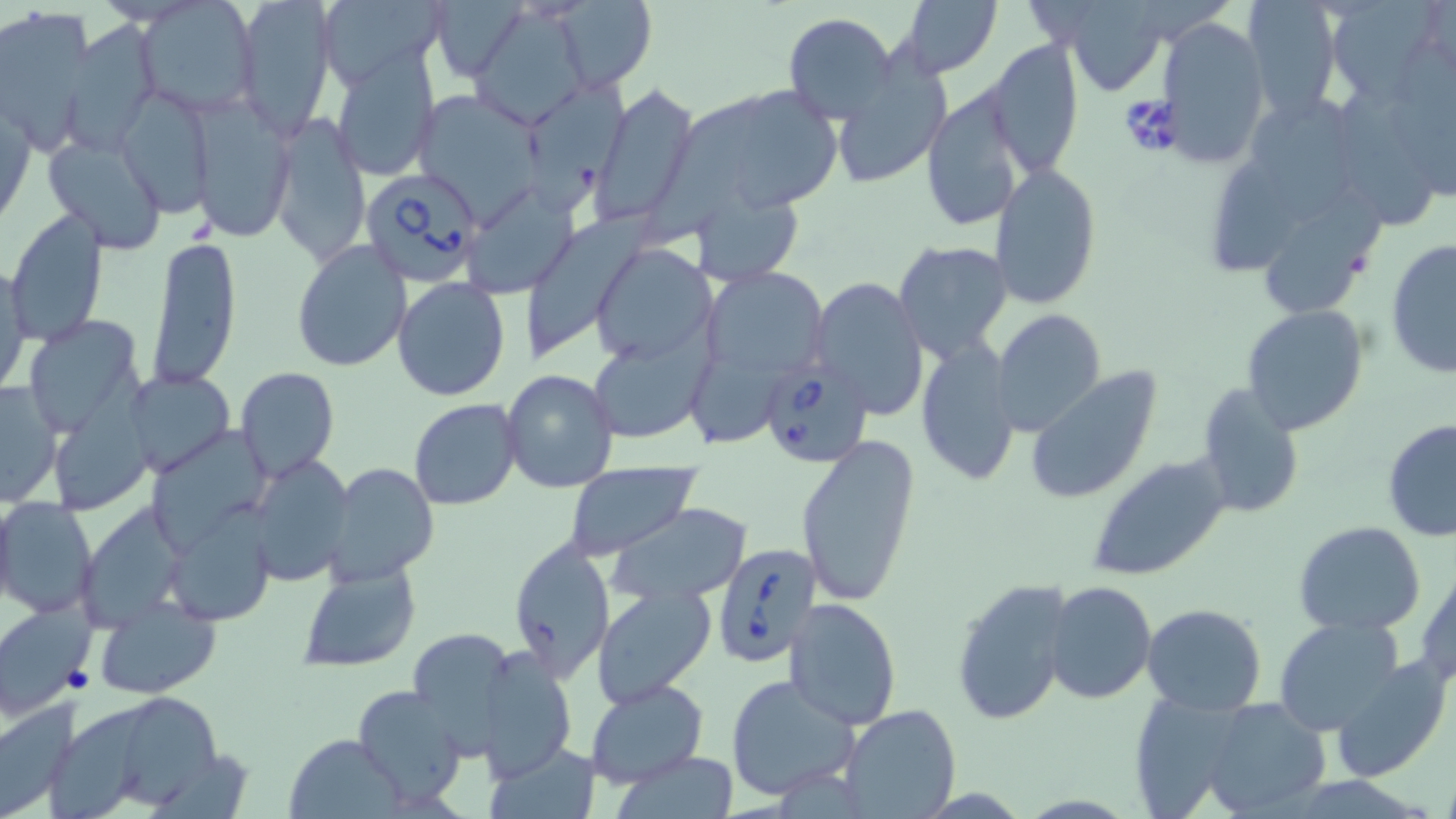
Summary:
  - Coordinate format: approximate bounding boxes as named x1/y1/x2/y2 corners in pixels
  - Uninfected red blood cell locations: (x1=135, y1=0, x2=263, y2=115), (x1=232, y1=0, x2=336, y2=140), (x1=318, y1=0, x2=442, y2=89), (x1=430, y1=0, x2=529, y2=83), (x1=547, y1=0, x2=658, y2=92), (x1=897, y1=0, x2=1002, y2=78), (x1=1239, y1=0, x2=1343, y2=119), (x1=1326, y1=0, x2=1450, y2=104), (x1=1050, y1=1, x2=1172, y2=94), (x1=470, y1=5, x2=590, y2=129), (x1=0, y1=8, x2=93, y2=154), (x1=784, y1=13, x2=898, y2=122), (x1=1155, y1=18, x2=1268, y2=165), (x1=62, y1=22, x2=159, y2=151), (x1=985, y1=39, x2=1083, y2=179), (x1=1391, y1=43, x2=1456, y2=200), (x1=333, y1=46, x2=441, y2=180), (x1=830, y1=56, x2=953, y2=190), (x1=520, y1=67, x2=628, y2=224), (x1=592, y1=82, x2=698, y2=223), (x1=114, y1=89, x2=214, y2=217), (x1=689, y1=89, x2=845, y2=212), (x1=921, y1=89, x2=1030, y2=231), (x1=425, y1=92, x2=541, y2=230), (x1=1337, y1=92, x2=1432, y2=229), (x1=0, y1=93, x2=35, y2=230), (x1=187, y1=97, x2=298, y2=243), (x1=1249, y1=98, x2=1353, y2=224), (x1=946, y1=101, x2=1090, y2=265), (x1=268, y1=112, x2=371, y2=268), (x1=42, y1=136, x2=167, y2=254), (x1=1211, y1=162, x2=1299, y2=272), (x1=989, y1=163, x2=1102, y2=309), (x1=459, y1=179, x2=579, y2=296), (x1=691, y1=185, x2=807, y2=287), (x1=1264, y1=188, x2=1387, y2=318), (x1=530, y1=211, x2=661, y2=363), (x1=6, y1=212, x2=111, y2=344), (x1=1386, y1=236, x2=1455, y2=380), (x1=146, y1=237, x2=241, y2=391), (x1=291, y1=240, x2=412, y2=372), (x1=893, y1=240, x2=1014, y2=363), (x1=590, y1=244, x2=717, y2=366), (x1=0, y1=257, x2=31, y2=402), (x1=703, y1=265, x2=828, y2=388), (x1=393, y1=276, x2=511, y2=400), (x1=809, y1=277, x2=930, y2=418), (x1=1240, y1=304, x2=1369, y2=434), (x1=991, y1=308, x2=1105, y2=436), (x1=23, y1=312, x2=147, y2=434), (x1=586, y1=331, x2=709, y2=447), (x1=916, y1=334, x2=1019, y2=485), (x1=692, y1=355, x2=782, y2=446), (x1=234, y1=366, x2=340, y2=480), (x1=501, y1=368, x2=621, y2=493), (x1=127, y1=369, x2=233, y2=477), (x1=1026, y1=369, x2=1164, y2=506), (x1=0, y1=380, x2=64, y2=508), (x1=1194, y1=383, x2=1306, y2=518), (x1=408, y1=398, x2=521, y2=510), (x1=1381, y1=420, x2=1456, y2=542), (x1=796, y1=431, x2=922, y2=608), (x1=1085, y1=451, x2=1233, y2=581), (x1=248, y1=454, x2=353, y2=588), (x1=327, y1=462, x2=438, y2=584), (x1=561, y1=464, x2=700, y2=561), (x1=1, y1=497, x2=98, y2=618), (x1=610, y1=503, x2=753, y2=602), (x1=164, y1=507, x2=275, y2=626), (x1=1295, y1=520, x2=1427, y2=637), (x1=507, y1=536, x2=616, y2=681), (x1=1416, y1=556, x2=1456, y2=689), (x1=297, y1=561, x2=419, y2=672), (x1=950, y1=576, x2=1076, y2=726), (x1=1045, y1=580, x2=1157, y2=702), (x1=592, y1=587, x2=716, y2=707), (x1=93, y1=597, x2=223, y2=697), (x1=788, y1=597, x2=901, y2=731), (x1=0, y1=601, x2=94, y2=716), (x1=1141, y1=603, x2=1268, y2=714), (x1=1272, y1=617, x2=1405, y2=735), (x1=407, y1=625, x2=522, y2=752), (x1=477, y1=643, x2=577, y2=779), (x1=1329, y1=655, x2=1453, y2=782), (x1=724, y1=673, x2=862, y2=804), (x1=584, y1=677, x2=708, y2=787), (x1=351, y1=685, x2=468, y2=805), (x1=1125, y1=690, x2=1251, y2=817), (x1=1201, y1=697, x2=1334, y2=819), (x1=0, y1=699, x2=78, y2=818), (x1=839, y1=705, x2=963, y2=819), (x1=286, y1=731, x2=403, y2=817), (x1=488, y1=743, x2=602, y2=819), (x1=614, y1=750, x2=740, y2=818)
  - Babesia divergens-infected red blood cell locations: (x1=358, y1=166, x2=486, y2=286), (x1=756, y1=359, x2=871, y2=467), (x1=713, y1=540, x2=819, y2=669)
  - Slide-level diagnosis: Babesia divergens
  - Stain: May-Grünwald-Giemsa
  - Field of view: single
  - Magnification: 1000x
  - Modality: light microscopy
  - Image size: 1456×819 pixels
  - Preparation: thin blood smear